Locate every Plasmodium falciparum-infected red blood cell.
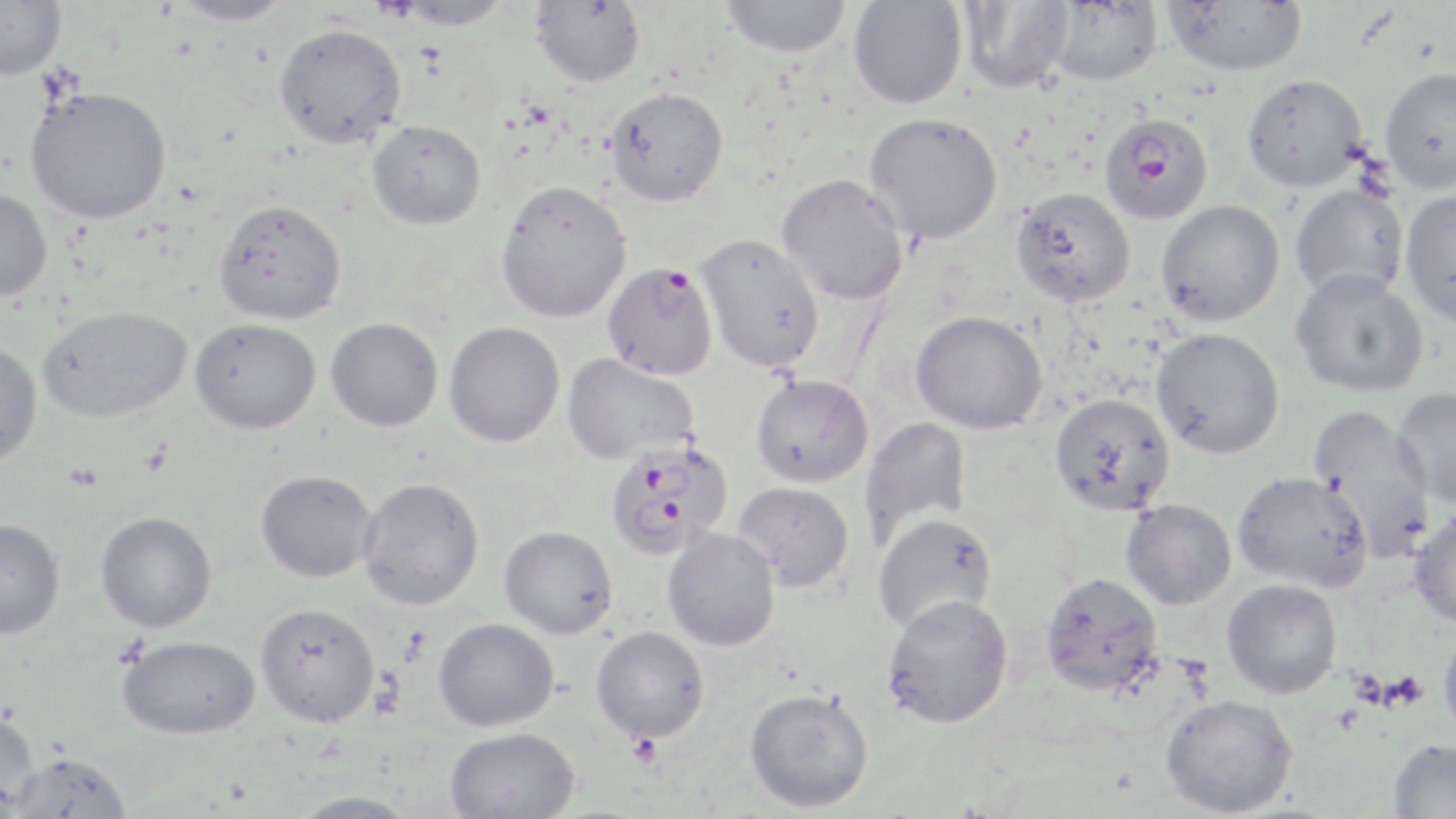
Approximate bounding boxes as named x1/y1/x2/y2 corners in pixels.
Plasmodium falciparum-infected red blood cells: (x1=1099, y1=112, x2=1212, y2=223), (x1=602, y1=262, x2=718, y2=382), (x1=604, y1=439, x2=732, y2=559).

{
  "slide_level_diagnosis": "Plasmodium falciparum",
  "platelet_locations": "approximate bounding boxes as named x1/y1/x2/y2 corners in pixels: (x1=1379, y1=669, x2=1429, y2=712), (x1=626, y1=732, x2=664, y2=769)",
  "field_of_view": "one of a larger specimen",
  "stain": "May-Grünwald-Giemsa",
  "modality": "light microscopy",
  "uninfected_red_blood_cell_locations": "approximate bounding boxes as named x1/y1/x2/y2 corners in pixels: (x1=173, y1=0, x2=292, y2=27), (x1=393, y1=0, x2=512, y2=29), (x1=719, y1=0, x2=854, y2=59), (x1=956, y1=0, x2=1074, y2=94), (x1=1045, y1=0, x2=1164, y2=85), (x1=0, y1=1, x2=66, y2=81), (x1=531, y1=1, x2=646, y2=87), (x1=848, y1=1, x2=967, y2=110), (x1=1162, y1=1, x2=1308, y2=77), (x1=273, y1=23, x2=406, y2=149), (x1=1379, y1=66, x2=1456, y2=194), (x1=1242, y1=74, x2=1368, y2=192), (x1=25, y1=86, x2=172, y2=224), (x1=605, y1=88, x2=728, y2=207), (x1=863, y1=112, x2=1003, y2=244), (x1=367, y1=120, x2=486, y2=230), (x1=776, y1=173, x2=910, y2=305), (x1=495, y1=180, x2=632, y2=323), (x1=1288, y1=183, x2=1410, y2=303), (x1=1010, y1=187, x2=1135, y2=307), (x1=0, y1=188, x2=52, y2=302), (x1=1399, y1=190, x2=1456, y2=327), (x1=213, y1=199, x2=346, y2=326), (x1=1155, y1=200, x2=1285, y2=327), (x1=695, y1=234, x2=826, y2=373), (x1=1289, y1=268, x2=1429, y2=398), (x1=38, y1=306, x2=191, y2=423), (x1=910, y1=310, x2=1048, y2=435), (x1=189, y1=318, x2=321, y2=434), (x1=326, y1=318, x2=443, y2=431), (x1=444, y1=322, x2=565, y2=447), (x1=1151, y1=328, x2=1285, y2=460), (x1=0, y1=344, x2=42, y2=466), (x1=562, y1=353, x2=700, y2=465), (x1=751, y1=374, x2=874, y2=488), (x1=1391, y1=387, x2=1456, y2=509), (x1=1049, y1=392, x2=1176, y2=516), (x1=1308, y1=405, x2=1437, y2=560), (x1=859, y1=417, x2=972, y2=550), (x1=255, y1=470, x2=378, y2=583), (x1=1232, y1=471, x2=1373, y2=593), (x1=357, y1=477, x2=484, y2=610), (x1=733, y1=481, x2=855, y2=591), (x1=1120, y1=499, x2=1237, y2=610), (x1=1407, y1=507, x2=1456, y2=628), (x1=95, y1=511, x2=217, y2=632), (x1=872, y1=514, x2=998, y2=633), (x1=0, y1=519, x2=65, y2=639), (x1=499, y1=525, x2=618, y2=639), (x1=663, y1=528, x2=780, y2=651), (x1=1040, y1=571, x2=1164, y2=696), (x1=1221, y1=579, x2=1343, y2=699), (x1=881, y1=594, x2=1013, y2=729), (x1=255, y1=602, x2=380, y2=728), (x1=434, y1=618, x2=559, y2=732), (x1=1438, y1=624, x2=1456, y2=742), (x1=591, y1=626, x2=709, y2=742), (x1=117, y1=635, x2=260, y2=740), (x1=744, y1=687, x2=874, y2=813), (x1=1159, y1=693, x2=1299, y2=817), (x1=0, y1=711, x2=40, y2=813), (x1=444, y1=726, x2=580, y2=819), (x1=1388, y1=739, x2=1456, y2=818), (x1=9, y1=752, x2=134, y2=818), (x1=286, y1=791, x2=420, y2=818)",
  "preparation": "thin blood smear",
  "image_size": "1456×819 pixels",
  "magnification": "1000x"
}